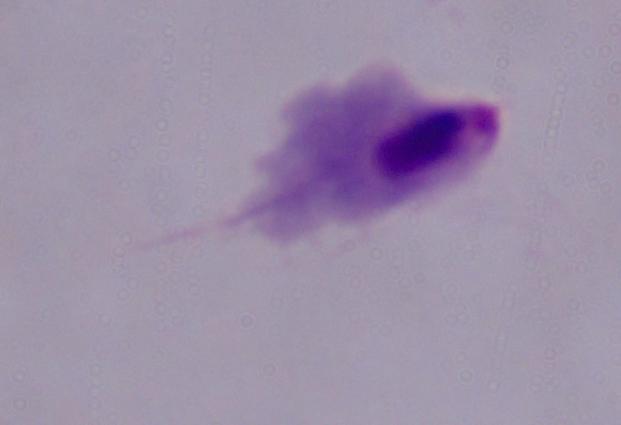
Summary:
  - Magnification: 1000x
  - Identification: trichomonad
  - Modality: photomicrograph